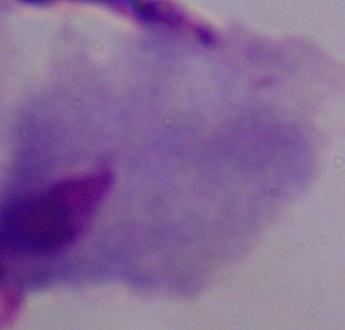

Summary:
  - Modality: micrograph
  - Identification: trichomonad
  - Magnification: 1000x